Locate platelets.
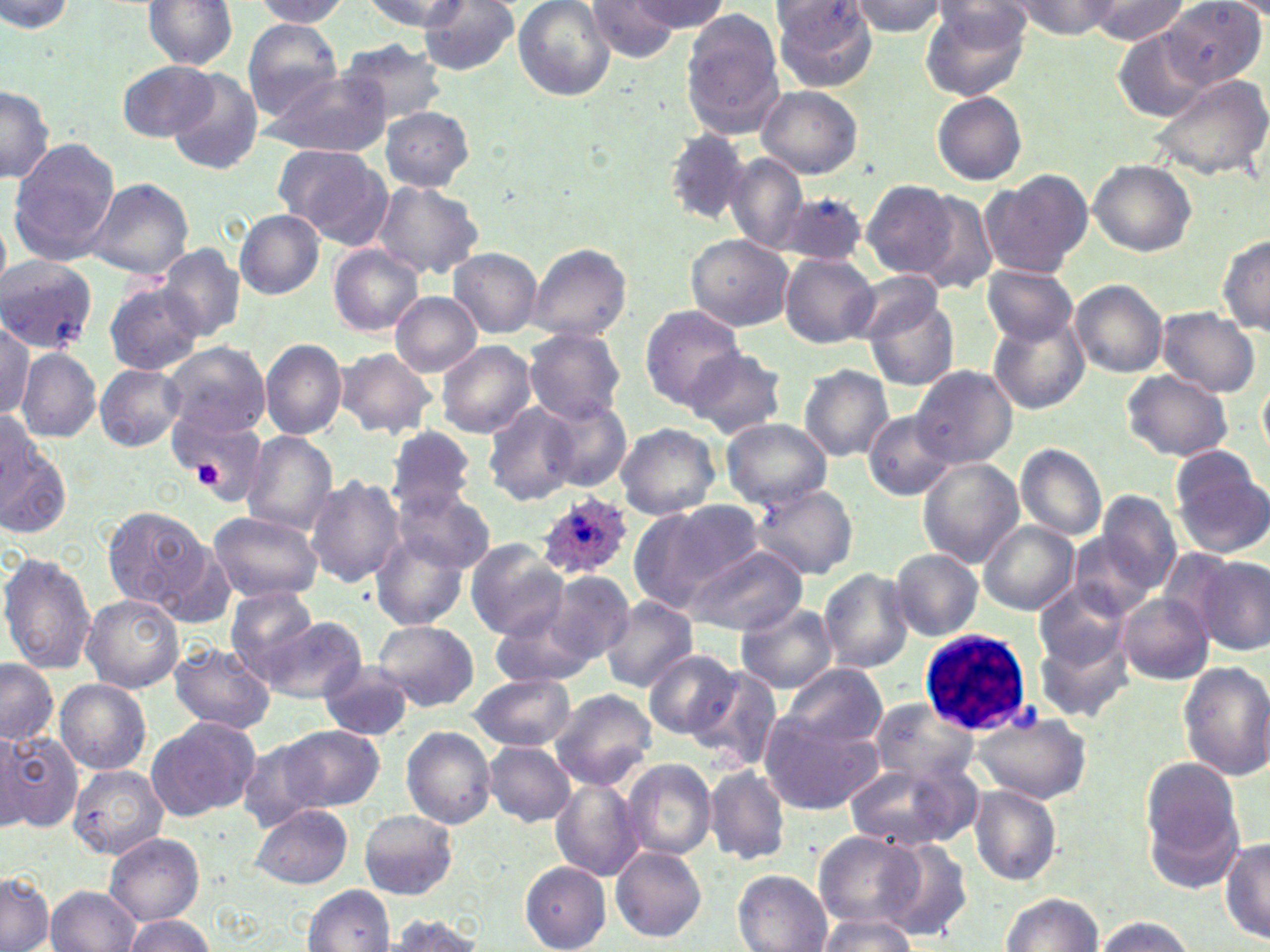
Approximate bounding boxes as (x1,y1)-(x2,y2) corner pairs in pixels.
Platelets: (194,461)-(223,487).

White blood cell locations: (919,626)-(1034,736). Plasmodium ovale-infected red blood cell locations: (534,488)-(633,579). Uninfected red blood cell locations: (143,0)-(239,69), (251,0)-(353,26), (362,0)-(470,32), (513,0)-(617,102), (585,0)-(677,61), (630,0)-(728,32), (771,0)-(880,90), (1162,0)-(1266,89), (848,1)-(949,36), (1009,1)-(1126,38), (1089,1)-(1186,44), (3,2)-(76,36), (418,3)-(518,80), (921,3)-(1027,101), (682,12)-(785,138), (241,19)-(345,115), (1112,28)-(1211,123), (338,38)-(448,128), (120,59)-(220,141), (261,67)-(391,157), (169,71)-(263,174), (1150,76)-(1270,183), (0,83)-(54,184), (755,86)-(861,178), (933,92)-(1027,184), (379,106)-(474,191), (666,131)-(751,221), (8,138)-(121,264), (271,144)-(388,242), (724,154)-(808,252), (1089,160)-(1197,256), (981,171)-(1092,278), (86,178)-(194,278), (863,180)-(960,278), (371,181)-(483,281), (909,190)-(1000,295), (780,192)-(869,265), (235,210)-(324,299), (1217,233)-(1270,336), (685,234)-(793,330), (156,244)-(246,342), (329,244)-(424,337), (528,244)-(631,342), (449,249)-(542,337), (781,254)-(879,347), (0,257)-(97,354), (981,265)-(1078,344), (853,271)-(942,343), (1070,279)-(1167,377), (104,281)-(203,375), (390,292)-(482,376), (866,292)-(959,390), (641,306)-(744,409), (1155,308)-(1262,398), (991,312)-(1090,414), (1,320)-(35,417), (524,328)-(626,425), (261,339)-(348,438), (437,341)-(535,436), (161,342)-(270,438), (687,346)-(788,438), (15,347)-(102,441), (335,348)-(438,437), (95,364)-(185,451), (799,364)-(894,462), (913,366)-(1016,468), (1121,370)-(1233,463), (1258,375)-(1270,465), (540,399)-(631,493), (168,400)-(269,495), (483,403)-(579,505), (864,410)-(956,501), (0,412)-(47,505), (722,418)-(832,508), (616,422)-(721,520), (387,425)-(476,515), (241,430)-(337,534), (0,434)-(72,537), (1015,444)-(1107,540), (1170,445)-(1270,557), (918,459)-(1023,567), (306,475)-(405,590), (746,483)-(857,580), (392,485)-(495,573), (1096,491)-(1181,592), (628,500)-(765,612), (103,507)-(212,612), (208,511)-(323,604), (978,520)-(1080,615), (372,531)-(468,629), (152,539)-(239,632), (466,539)-(568,640), (687,544)-(804,635), (891,549)-(982,640), (1,550)-(95,674), (1197,554)-(1269,656), (819,567)-(915,673), (540,569)-(635,664), (1034,580)-(1132,677), (227,585)-(319,679), (1118,593)-(1214,685), (80,595)-(184,693), (600,597)-(699,692), (737,602)-(838,693), (490,603)-(601,690), (262,615)-(365,703), (373,621)-(478,711), (1038,635)-(1133,724), (169,643)-(276,735), (645,650)-(740,739), (0,660)-(58,746), (1179,660)-(1269,778), (318,664)-(416,740), (780,664)-(891,752), (688,666)-(784,773), (469,674)-(575,751), (54,679)-(151,774), (548,688)-(657,789), (870,697)-(982,788), (757,711)-(881,815), (975,712)-(1091,802), (146,718)-(260,822), (257,724)-(385,819), (402,726)-(497,829), (0,729)-(82,833), (484,741)-(576,826), (621,758)-(718,863), (1141,758)-(1243,862), (845,760)-(976,852), (68,764)-(168,861), (706,764)-(790,865), (551,778)-(644,881), (969,786)-(1062,885), (248,804)-(351,889), (359,809)-(458,899), (814,831)-(924,930), (105,834)-(203,924), (883,838)-(974,941), (1221,839)-(1270,944), (611,846)-(707,943), (520,861)-(611,952), (733,870)-(831,951), (0,871)-(54,952), (302,883)-(395,951), (47,885)-(140,952), (1000,894)-(1103,951), (384,913)-(486,951), (120,915)-(217,952), (815,916)-(918,952), (1095,916)-(1195,952). Slide-level diagnosis: Plasmodium ovale. Captured at 1000x magnification. May-Grünwald-Giemsa stain. Image is 1270×952 pixels. Thin blood smear. Light microscopy. One field of a larger specimen.